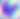

Captured at 400x magnification. Toxoplasma gondii is shown. Micrograph.